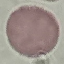

Summary:
  - Result: no malaria parasites detected
  - Preparation: thin blood film
  - Capture: smartphone camera at the microscope eyepiece
  - Image type: cell patch, automatically extracted from a larger field of view and resized to 64 × 64 pixels
  - Stain: Giemsa